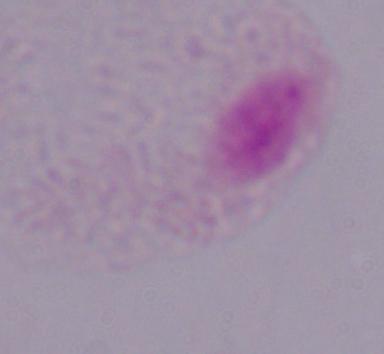
Summary:
  - Identification: trichomonad
  - Modality: photomicrograph
  - Magnification: 1000x